Assess this cell for malaria.
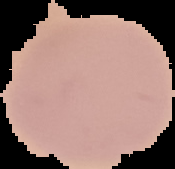

It is uninfected.

From a thin blood smear. Segmented cell region on a black background. Image is 175×169 pixels.